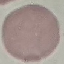

Summary:
  - Malaria status: uninfected
  - Preparation: thin smear
  - Stain: Giemsa
  - Capture: smartphone camera at the microscope eyepiece
  - Image type: automatically extracted cell patch, resized to 64 × 64 pixels